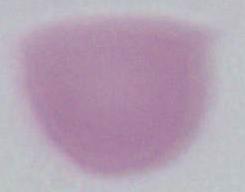
magnification = 1000x
identification = red blood cell
modality = photomicrograph